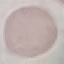

Summary:
  - Result: negative for malaria parasites
  - Capture: smartphone through the microscope eyepiece
  - Stain: Giemsa
  - Preparation: thin blood film
  - Image type: automatically extracted cell patch, resized to 64 × 64 pixels